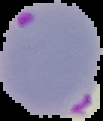
image type = cell region segmented out of the field of view; surrounding area masked to black
result = Plasmodium parasites detected
preparation = thin blood smear
image size = 103×121 pixels